Identify the blood parasite species.
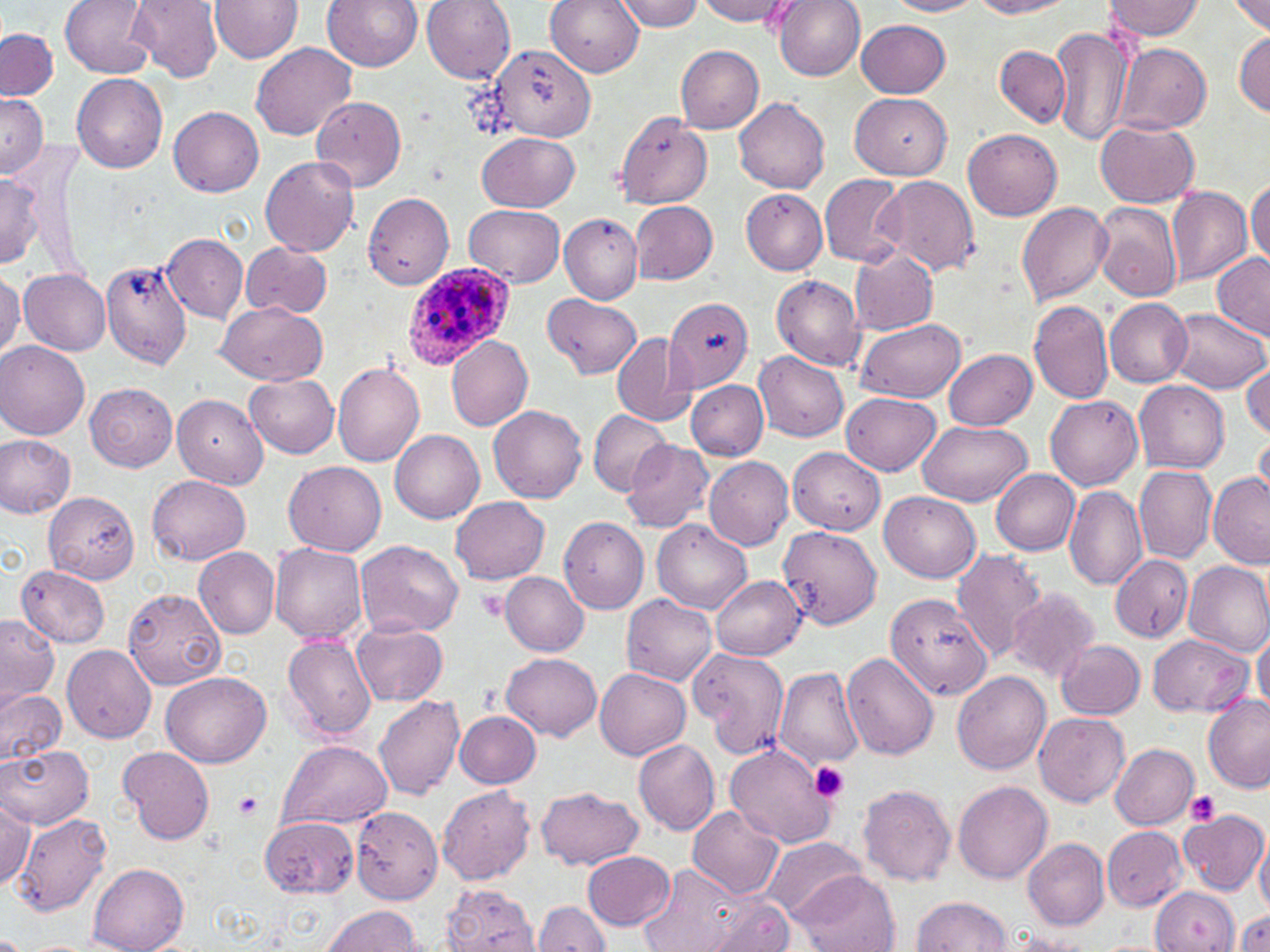

Plasmodium ovale.

Summary:
  - Coordinate format: approximate bounding boxes as [x1, y1, x2, y2] in pixels
  - Platelet locations: [478, 589, 510, 624], [807, 759, 852, 804], [235, 790, 264, 820], [1186, 790, 1220, 826]
  - Uninfected red blood cell locations: [60, 0, 155, 77], [129, 0, 224, 81], [210, 0, 304, 62], [323, 0, 422, 71], [546, 0, 644, 75], [614, 0, 703, 31], [697, 0, 792, 24], [774, 0, 867, 81], [887, 0, 983, 17], [971, 0, 1076, 18], [1102, 0, 1204, 40], [423, 1, 516, 83], [1231, 1, 1270, 35], [855, 19, 950, 98], [1050, 22, 1132, 147], [1, 29, 57, 101], [1234, 30, 1269, 116], [252, 42, 357, 141], [1113, 42, 1212, 134], [487, 43, 594, 140], [675, 46, 765, 133], [995, 46, 1070, 128], [72, 72, 168, 173], [0, 92, 48, 177], [849, 92, 952, 178], [311, 96, 407, 192], [734, 97, 830, 194], [169, 106, 264, 196], [613, 113, 712, 208], [1096, 121, 1200, 207], [963, 129, 1062, 220], [478, 132, 580, 212], [261, 156, 359, 258], [820, 172, 908, 267], [0, 173, 43, 266], [877, 175, 980, 277], [1246, 178, 1269, 263], [1166, 186, 1252, 285], [741, 189, 828, 275], [363, 192, 454, 290], [630, 201, 718, 284], [1091, 201, 1183, 301], [1017, 202, 1112, 306], [465, 204, 564, 286], [559, 214, 643, 303], [161, 234, 248, 323], [240, 241, 331, 318], [850, 248, 937, 337], [1211, 250, 1270, 337], [95, 255, 194, 368], [19, 269, 110, 355], [0, 270, 23, 361], [772, 274, 866, 371], [543, 293, 641, 379], [663, 296, 754, 393], [1105, 298, 1192, 387], [215, 300, 327, 385], [1028, 300, 1114, 405], [1167, 307, 1268, 393], [855, 318, 967, 402], [610, 333, 698, 426], [447, 334, 534, 431], [0, 341, 90, 441], [944, 348, 1037, 430], [755, 351, 849, 443], [332, 360, 426, 466], [1242, 363, 1270, 440], [245, 374, 339, 458], [685, 378, 769, 459], [1134, 379, 1230, 473], [85, 381, 178, 471], [841, 392, 940, 475], [172, 395, 268, 488], [1045, 396, 1142, 490], [488, 405, 588, 503], [587, 409, 673, 496], [918, 420, 1034, 507], [390, 429, 485, 524], [1253, 430, 1270, 506], [0, 436, 75, 518], [620, 440, 713, 531], [788, 446, 884, 534], [704, 456, 795, 550], [283, 461, 387, 556], [1133, 466, 1217, 563], [992, 470, 1079, 555], [1208, 472, 1270, 567], [148, 473, 252, 565], [1064, 486, 1146, 590], [42, 490, 140, 582], [880, 490, 980, 581], [451, 496, 550, 584], [559, 516, 650, 614], [652, 520, 751, 613], [779, 520, 880, 631], [355, 540, 463, 639], [271, 543, 369, 644], [193, 546, 280, 639], [952, 548, 1049, 661], [1110, 554, 1193, 643], [1184, 561, 1270, 656], [16, 565, 110, 647], [500, 571, 588, 655], [711, 574, 806, 659], [1006, 587, 1099, 682], [125, 589, 227, 689], [885, 593, 991, 699], [622, 594, 718, 687], [0, 613, 59, 706], [350, 618, 449, 706], [1253, 630, 1270, 716], [1148, 633, 1253, 717], [281, 634, 376, 742], [1055, 638, 1145, 720], [61, 644, 157, 744], [693, 648, 788, 762], [500, 652, 602, 738], [843, 652, 940, 760], [773, 664, 865, 770], [595, 668, 690, 760], [160, 670, 274, 769], [954, 672, 1050, 774], [0, 688, 66, 768], [1201, 695, 1269, 792], [373, 696, 466, 803], [455, 711, 541, 789], [1035, 712, 1132, 805], [633, 739, 720, 835], [277, 740, 391, 831], [0, 744, 93, 830], [725, 744, 838, 847], [1110, 744, 1199, 829], [118, 747, 213, 846], [955, 781, 1053, 883], [858, 784, 956, 885], [437, 785, 535, 885], [537, 787, 643, 870], [1, 791, 35, 889], [687, 805, 784, 899], [351, 807, 443, 904], [1176, 808, 1268, 896], [12, 811, 114, 916], [259, 817, 358, 896], [1102, 827, 1187, 910], [1255, 834, 1270, 920], [762, 835, 866, 921], [1025, 838, 1110, 929], [583, 851, 675, 930], [639, 862, 764, 952], [88, 863, 190, 952], [795, 871, 899, 951], [442, 884, 538, 952], [1150, 886, 1240, 951], [911, 896, 1011, 951], [702, 899, 796, 952], [534, 900, 610, 951], [322, 904, 423, 952], [1231, 909, 1270, 952]
  - Plasmodium ovale-infected red blood cell locations: [400, 260, 521, 371]
  - Field of view: single
  - Modality: optical microscopy
  - Preparation: thin blood smear
  - Image size: 1270×952 pixels
  - Stain: May-Grünwald-Giemsa
  - Magnification: 1000x